Assess the morphology of the red blood cells.
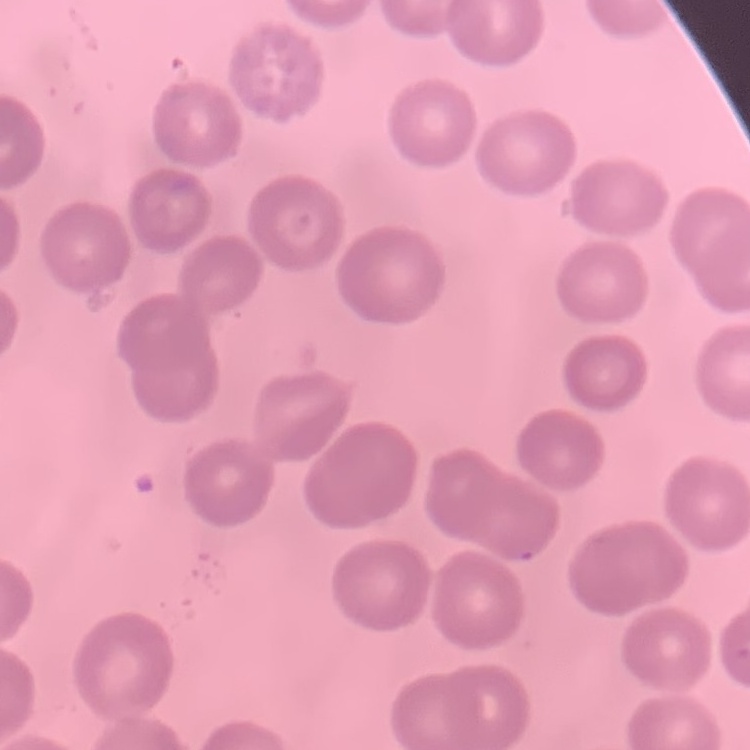

No rouleaux formation.

Summary:
  - Image type: one tile cut from a larger photomicrograph
  - Stain: Field's or Giemsa
  - Preparation: thin blood film